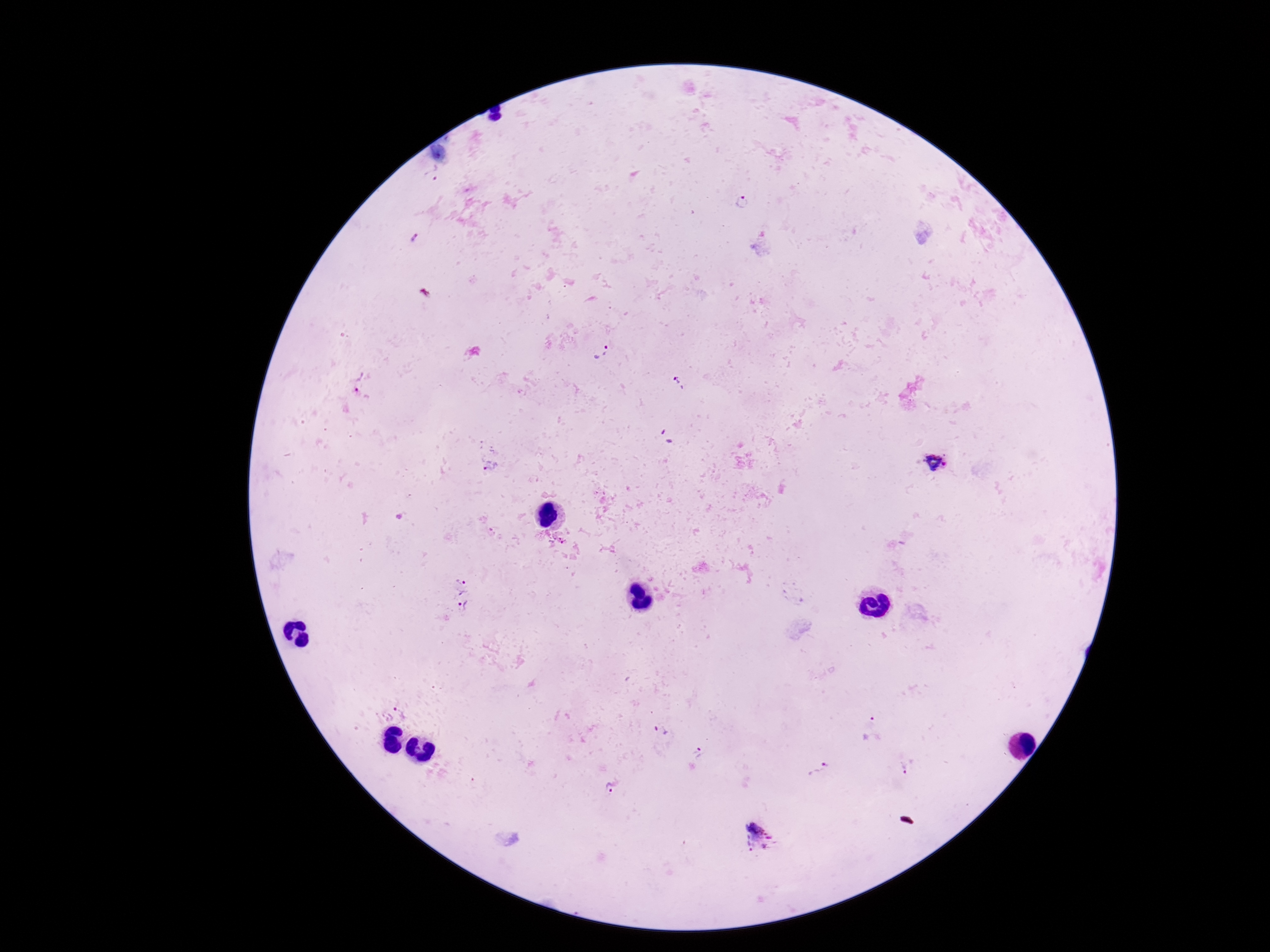
Approximate object centers, in pixels from the top-left corner.
Summary:
  - Plasmodium parasite locations: (x=742, y=202), (x=415, y=240), (x=600, y=349), (x=360, y=383), (x=678, y=384), (x=668, y=438), (x=935, y=463), (x=490, y=466), (x=557, y=537), (x=460, y=583), (x=462, y=607), (x=393, y=714), (x=871, y=726), (x=661, y=730), (x=698, y=754), (x=819, y=768), (x=907, y=768), (x=608, y=788), (x=760, y=837)
  - Field of view: one from this slide
  - Image size: 1270×952 pixels
  - Patient malaria status: infected
  - Stain: Giemsa
  - Preparation: thick peripheral-blood smear
  - Magnification: 100x
  - Capture: smartphone camera through the microscope eyepiece